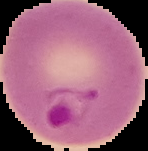
Malaria status: parasitized. Image is 148×151 pixels. From a thin blood film. The area outside the segmented cell region is set to black.